Assess this cell for malaria.
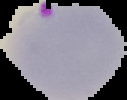
It is parasitized.

From a thin blood film. Image is 127×100 pixels. Cell region segmented out of the field of view; the surrounding area is masked to black.